Mark where leukocytes are.
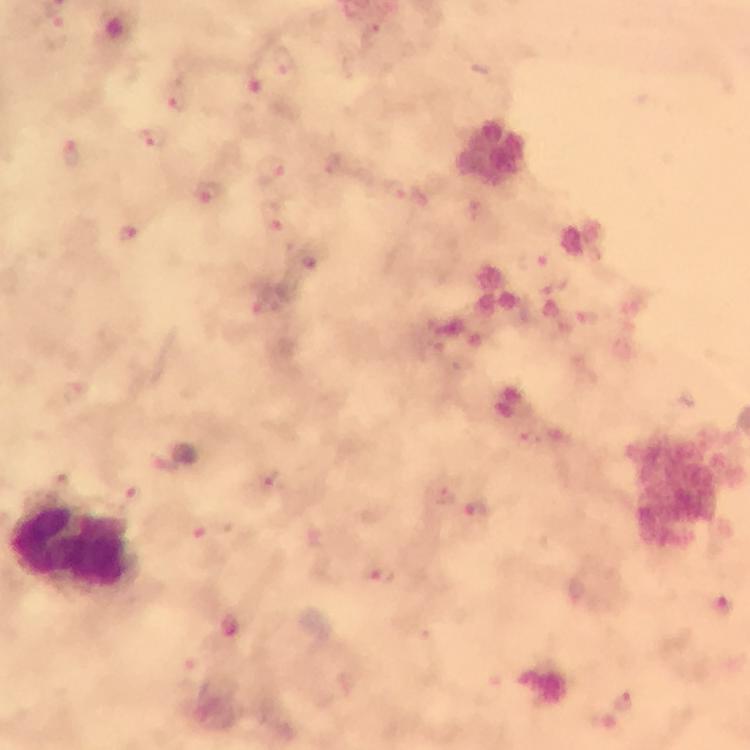

Approximate object centers, in pixels from the top-left corner.
Leukocytes: (x=72, y=544).

Plasmodium parasite locations: (x=254, y=78), (x=174, y=95), (x=152, y=139), (x=73, y=153), (x=271, y=169), (x=395, y=191), (x=206, y=194), (x=273, y=215), (x=130, y=233), (x=534, y=260), (x=314, y=267), (x=262, y=295), (x=273, y=483), (x=479, y=512), (x=202, y=529), (x=378, y=575), (x=721, y=606), (x=231, y=632), (x=624, y=701). From a malaria diagnostic workup. Thick blood film. Image is 750×750 pixels. Photographed through the microscope with a smartphone camera. At 100x magnification. Immersion oil was used. Giemsa stain. A crop from one field of view.